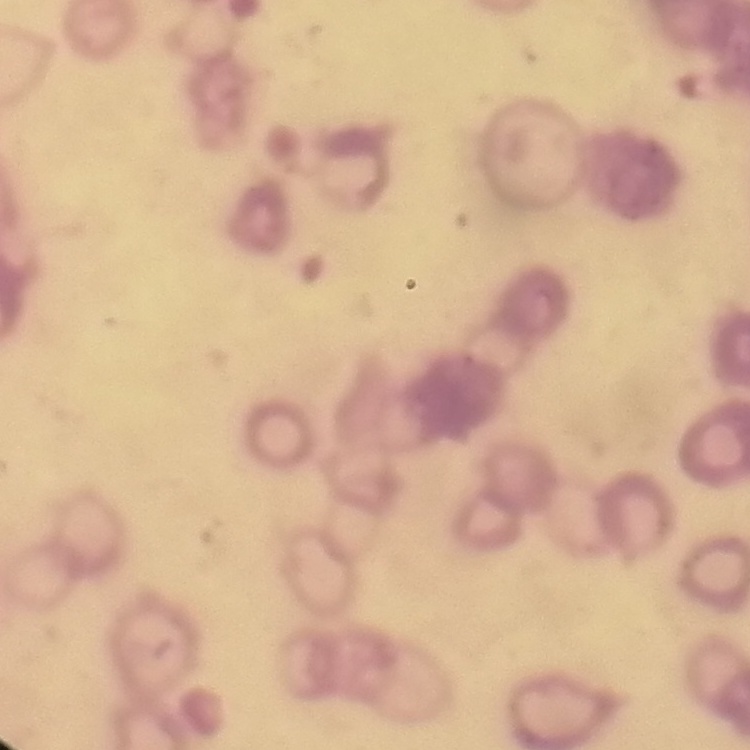

erythrocyte morphology = rouleaux formation
stain = Field's or Giemsa
preparation = thin peripheral smear
image type = square crop of a larger photomicrograph